Evaluate for parasitized red blood cells.
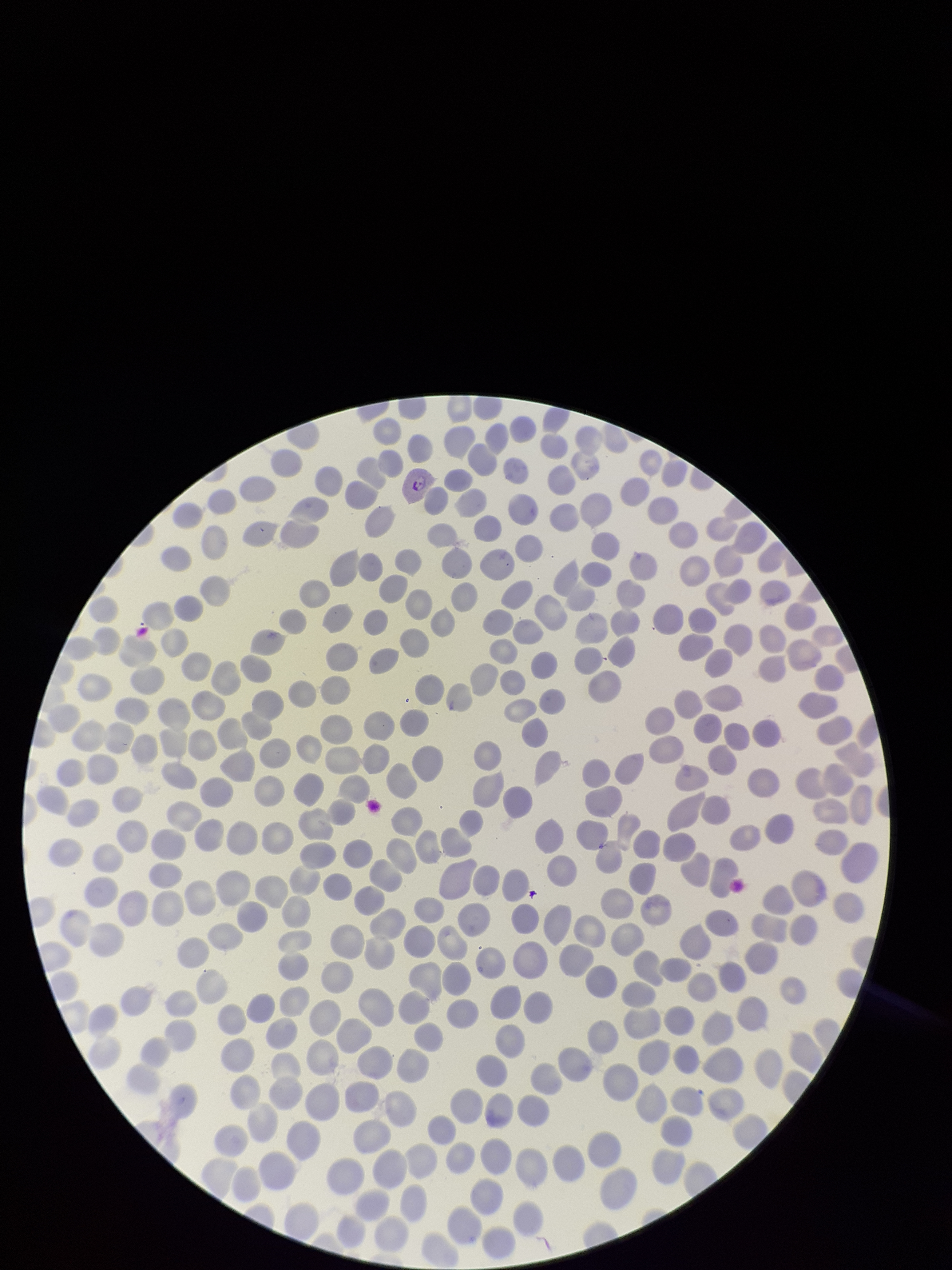

Identified.

Summary:
  - Stain: Giemsa
  - Image size: 952×1270 pixels
  - Red blood cell count: 328
  - Parasitized red blood cell count: 1
  - Preparation: thin
  - Capture: smartphone photograph through the microscope eyepiece
  - Field of view: one from this slide
  - Species reported for this patient: Plasmodium vivax
  - Patient malaria status: positive